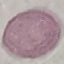

Malaria status: uninfected. Giemsa stain. Cell patch, automatically extracted from a larger field of view and resized to 64 × 64 pixels. Thin blood smear. Acquired by smartphone through the microscope eyepiece.